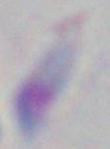

Photomicrograph. Toxoplasma gondii is seen. Captured at 1000x magnification.